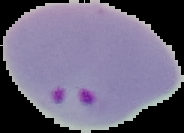

From a thin blood film. Image is 184×133 pixels. The area outside the segmented cell region is set to black. Malaria status: parasitized.